Classify this cell by malaria status.
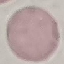

It is uninfected.

Summary:
  - Preparation: thin blood smear
  - Stain: Giemsa
  - Capture: smartphone camera at the microscope eyepiece
  - Image type: cell patch, automatically extracted from a larger field of view and resized to 64 × 64 pixels